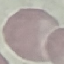
malaria_status: uninfected
stain: Giemsa
capture: smartphone camera at the microscope eyepiece
image_type: cell patch, automatically extracted from a larger field of view and resized to 64 × 64 pixels
preparation: thin blood film